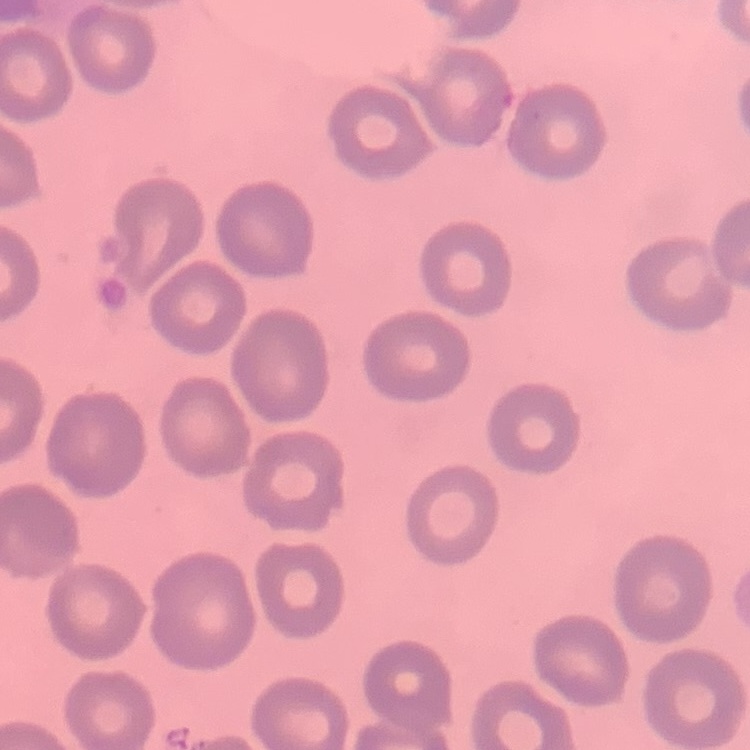
{
  "erythrocyte_morphology": "no rouleaux formation",
  "preparation": "thin blood smear",
  "stain": "Field's or Giemsa",
  "image_type": "one tile cut from a larger photomicrograph"
}